State which parasite is depicted.
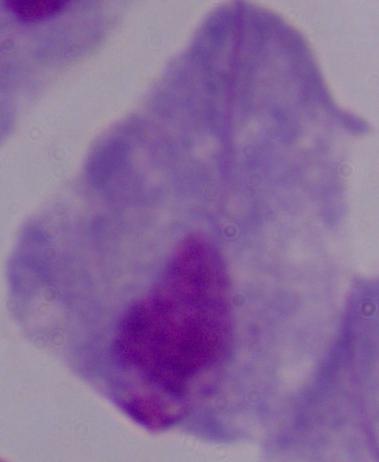
A trichomonad.

Summary:
  - Modality: micrograph
  - Magnification: 1000x